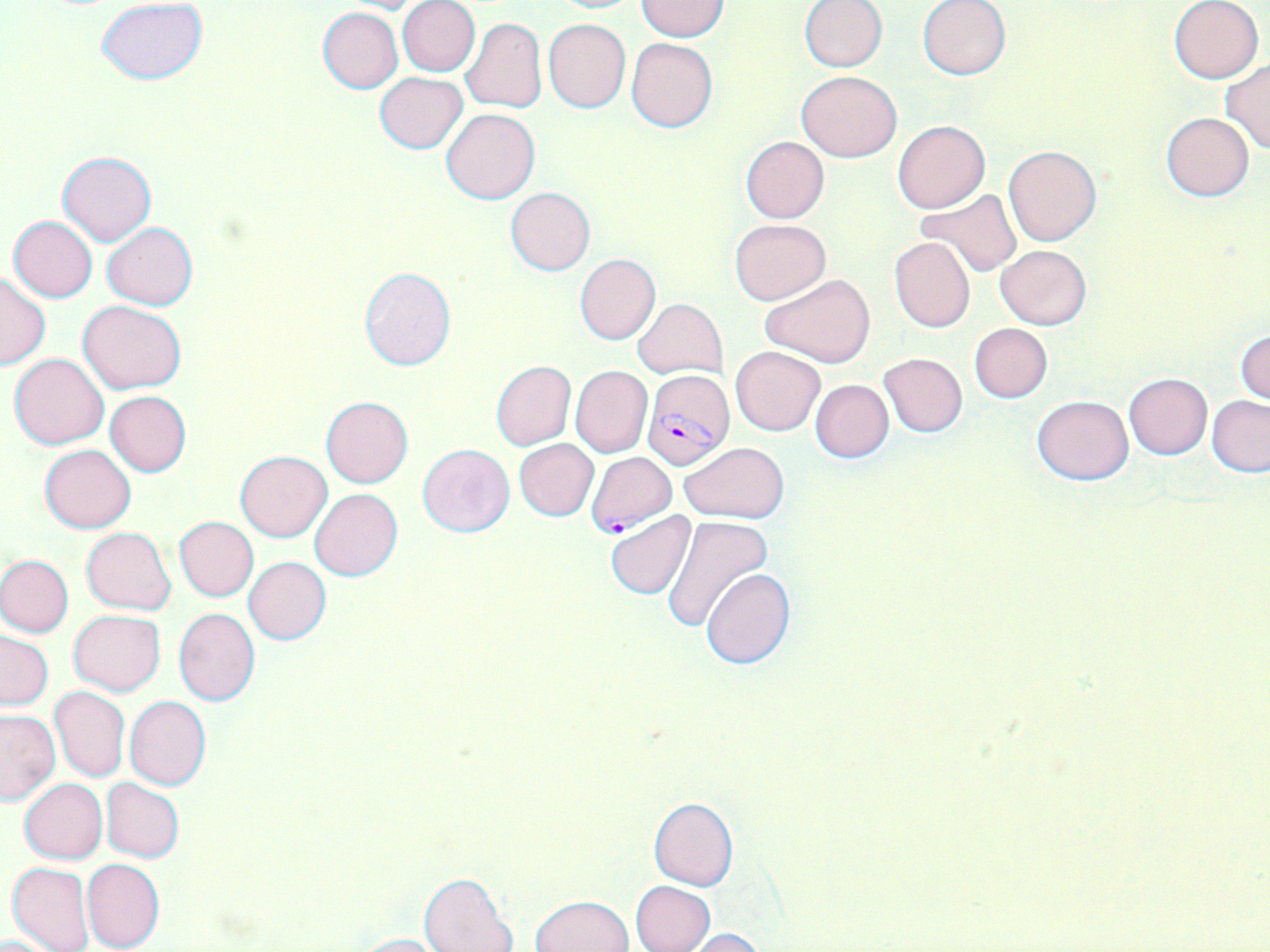

Plasmodium falciparum-infected red blood cell locations = approximate bounding boxes as (x1, y1, x2, y2) in pixels: (642, 369, 734, 471), (585, 452, 676, 535)
slide-level diagnosis = Plasmodium falciparum
stain = May-Grünwald-Giemsa
modality = light microscopy
preparation = thin blood smear
magnification = 1000x
uninfected red blood cell locations = approximate bounding boxes as (x1, y1, x2, y2) in pixels: (97, 0, 209, 84), (549, 0, 644, 13), (800, 0, 887, 71), (917, 0, 1011, 81), (334, 1, 437, 15), (397, 1, 480, 76), (635, 1, 729, 41), (1169, 1, 1264, 84), (318, 7, 403, 93), (460, 18, 546, 113), (543, 18, 630, 112), (626, 37, 717, 132), (1220, 60, 1270, 154), (796, 71, 902, 163), (375, 73, 468, 152), (441, 109, 540, 204), (1161, 113, 1254, 200), (893, 120, 989, 214), (740, 136, 829, 224), (1003, 144, 1101, 246), (58, 150, 156, 246), (506, 187, 596, 275), (915, 189, 1021, 277), (8, 216, 97, 303), (729, 219, 831, 305), (102, 222, 197, 310), (889, 238, 975, 332), (995, 244, 1093, 329), (575, 254, 661, 344), (359, 267, 457, 372), (0, 272, 50, 369), (759, 274, 878, 368), (632, 298, 727, 379), (78, 300, 187, 393), (969, 323, 1052, 403), (1235, 329, 1270, 407), (731, 345, 826, 437), (9, 352, 110, 449), (879, 352, 967, 437), (490, 360, 576, 449), (570, 365, 652, 458), (1124, 374, 1212, 458), (809, 379, 894, 463), (105, 391, 191, 476), (1032, 395, 1133, 485), (1207, 395, 1270, 476), (321, 397, 413, 488), (514, 438, 598, 520), (679, 440, 789, 523), (416, 444, 515, 536), (39, 445, 137, 533), (234, 450, 333, 542), (310, 489, 402, 580), (605, 512, 696, 599), (662, 515, 772, 631), (174, 516, 258, 601), (81, 527, 177, 613), (0, 554, 74, 638), (244, 557, 331, 644), (700, 568, 797, 670), (174, 608, 260, 706), (69, 609, 165, 696), (1, 631, 53, 710), (50, 686, 129, 783), (124, 696, 211, 791), (0, 710, 60, 804), (19, 778, 107, 864), (101, 779, 185, 862), (648, 797, 739, 891), (81, 858, 164, 951), (6, 862, 94, 952), (419, 873, 519, 952), (629, 880, 715, 951), (530, 895, 634, 952), (678, 928, 768, 952), (350, 933, 458, 952)
field of view = single
image size = 1270×952 pixels